Name the cell type shown.
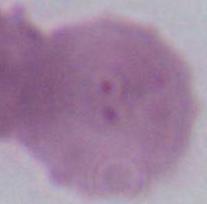
This is an erythrocyte.

magnification = 1000x
modality = photomicrograph